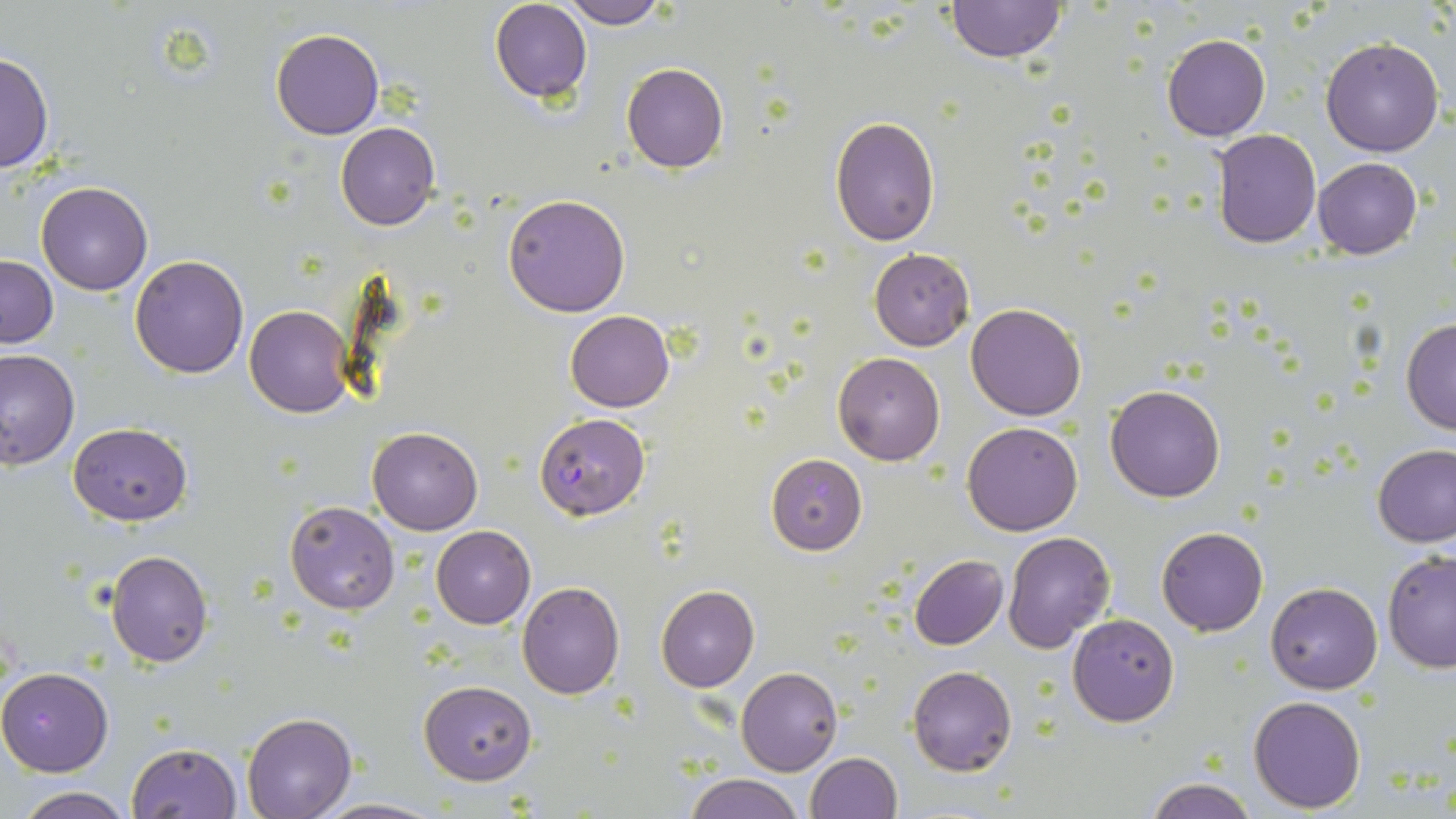
slide-level diagnosis = Plasmodium falciparum
uninfected red blood cell locations = approximate bounding boxes as (x1, y1, x2, y2) in pixels: (941, 0, 1068, 64), (490, 1, 592, 103), (556, 1, 668, 28), (271, 28, 383, 140), (1162, 33, 1271, 141), (1319, 37, 1446, 157), (0, 52, 53, 174), (621, 63, 729, 173), (830, 116, 940, 246), (335, 122, 439, 231), (1212, 129, 1321, 248), (1313, 157, 1423, 260), (36, 181, 153, 295), (503, 194, 632, 317), (869, 249, 974, 350), (130, 254, 248, 377), (1, 255, 58, 348), (966, 303, 1087, 421), (243, 305, 355, 418), (566, 311, 674, 412), (1401, 319, 1456, 433), (0, 349, 79, 470), (833, 352, 944, 465), (1104, 383, 1225, 504), (963, 422, 1083, 536), (68, 423, 193, 525), (367, 425, 482, 535), (1373, 444, 1456, 547), (766, 454, 868, 555), (285, 501, 400, 614), (431, 526, 536, 628), (1157, 526, 1268, 636), (1001, 532, 1116, 652), (105, 549, 213, 667), (1381, 550, 1456, 672), (910, 555, 1008, 649), (518, 581, 624, 699), (1266, 581, 1382, 694), (655, 585, 759, 692), (1067, 612, 1180, 726), (908, 665, 1017, 776), (736, 666, 842, 776), (0, 667, 112, 776), (420, 680, 537, 784), (1249, 695, 1366, 812), (243, 710, 356, 818), (126, 742, 244, 818), (805, 752, 901, 819), (683, 773, 803, 819), (1144, 777, 1259, 818), (13, 788, 133, 819), (313, 798, 442, 817)
image size = 1456×819 pixels
modality = light microscopy
preparation = thin blood smear
magnification = 1000x
field of view = single
stain = May-Grünwald-Giemsa
Plasmodium falciparum-infected red blood cell locations = approximate bounding boxes as (x1, y1, x2, y2) in pixels: (534, 414, 650, 519)